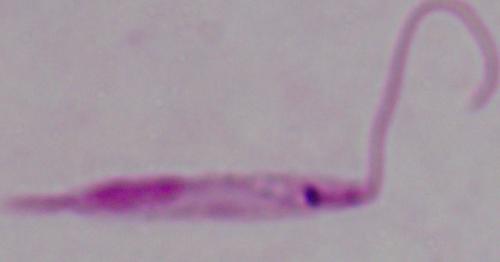
1000x magnification. Micrograph. A Leishmania parasite is shown.